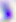
Summary:
  - Modality: micrograph
  - Magnification: 400x
  - Identification: Toxoplasma gondii